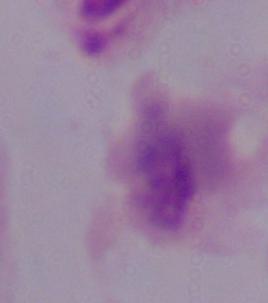 A trichomonad is seen. Micrograph. 1000x magnification.